State which cell type is depicted.
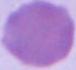
This is an erythrocyte.

Summary:
  - Modality: micrograph
  - Magnification: 1000x